Outline each Plasmodium falciparum-infected red blood cell.
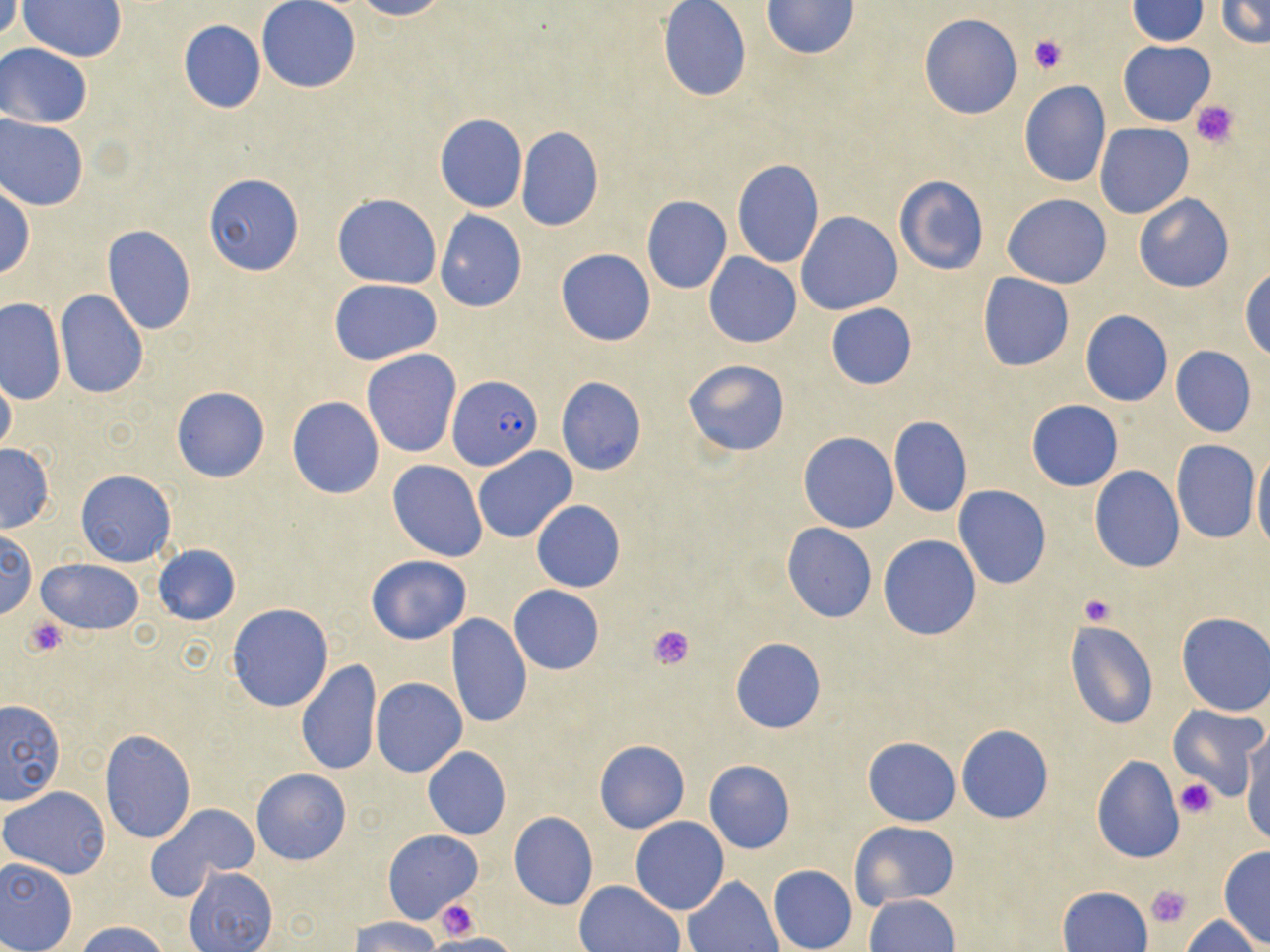

Approximate bounding boxes as [x1, y1, x2, y2] in pixels.
Plasmodium falciparum-infected red blood cells: [447, 375, 543, 468].

{
  "slide_level_diagnosis": "Plasmodium falciparum",
  "preparation": "thin blood film",
  "magnification": "1000x",
  "uninfected_red_blood_cell_locations": "approximate bounding boxes as [x1, y1, x2, y2] in pixels: [0, 0, 22, 45], [257, 0, 361, 93], [350, 0, 449, 21], [1125, 0, 1210, 44], [1215, 0, 1269, 49], [18, 1, 127, 61], [762, 1, 862, 58], [658, 2, 750, 102], [920, 13, 1022, 119], [178, 19, 267, 114], [1118, 40, 1216, 126], [1, 44, 92, 127], [1019, 80, 1112, 186], [435, 113, 527, 212], [0, 114, 89, 211], [1096, 123, 1193, 218], [515, 126, 604, 232], [731, 159, 825, 268], [202, 174, 304, 275], [895, 176, 988, 275], [0, 183, 34, 280], [333, 193, 442, 288], [1003, 194, 1112, 288], [1134, 194, 1235, 292], [641, 195, 732, 294], [435, 210, 527, 312], [798, 211, 901, 314], [102, 225, 196, 336], [556, 249, 655, 346], [703, 253, 801, 348], [1240, 268, 1270, 358], [978, 273, 1074, 372], [329, 278, 443, 365], [56, 289, 148, 398], [0, 296, 65, 404], [825, 303, 917, 389], [1080, 310, 1174, 406], [1169, 346, 1255, 437], [361, 348, 461, 458], [683, 359, 790, 458], [0, 370, 17, 457], [554, 376, 646, 475], [171, 386, 270, 482], [287, 396, 384, 499], [1026, 399, 1124, 492], [887, 415, 973, 517], [799, 431, 898, 532], [1171, 440, 1259, 544], [0, 444, 55, 532], [1251, 445, 1270, 555], [473, 447, 578, 544], [388, 460, 487, 560], [1089, 467, 1185, 572], [75, 469, 176, 566], [953, 486, 1051, 589], [531, 500, 625, 592], [782, 523, 876, 623], [1, 529, 37, 620], [877, 535, 982, 640], [151, 545, 240, 625], [366, 556, 471, 644], [37, 559, 144, 635], [508, 585, 605, 675], [226, 603, 333, 713], [1175, 612, 1270, 716], [447, 614, 532, 729], [1063, 620, 1158, 729], [729, 638, 826, 734], [296, 660, 383, 778], [371, 677, 467, 778], [0, 699, 68, 806], [1166, 705, 1266, 801], [955, 725, 1054, 823], [99, 729, 195, 845], [1240, 735, 1269, 847], [862, 736, 959, 827], [595, 739, 689, 834], [421, 746, 511, 840], [1092, 754, 1185, 862], [703, 760, 795, 853], [251, 769, 352, 866], [2, 785, 112, 878], [145, 804, 258, 902], [509, 812, 598, 910], [630, 817, 729, 915], [850, 821, 960, 911], [383, 830, 482, 924], [1217, 846, 1270, 946], [0, 855, 79, 952], [768, 864, 857, 952], [184, 866, 276, 951], [683, 875, 784, 952], [575, 880, 684, 951], [1058, 886, 1153, 952], [866, 894, 960, 952], [1181, 914, 1261, 951], [350, 917, 441, 951], [77, 921, 169, 952], [423, 932, 522, 952]",
  "stain": "May-Grünwald-Giemsa",
  "modality": "light microscopy",
  "platelet_locations": "approximate bounding boxes as [x1, y1, x2, y2] in pixels: [1029, 34, 1068, 75], [1190, 99, 1241, 148], [1079, 593, 1116, 625], [22, 615, 68, 658], [648, 622, 697, 669], [1174, 777, 1217, 819], [1144, 886, 1192, 929], [435, 898, 480, 939]",
  "image_size": "1270×952 pixels",
  "field_of_view": "one of a larger specimen"
}